Locate every blood parasite and identify its species.
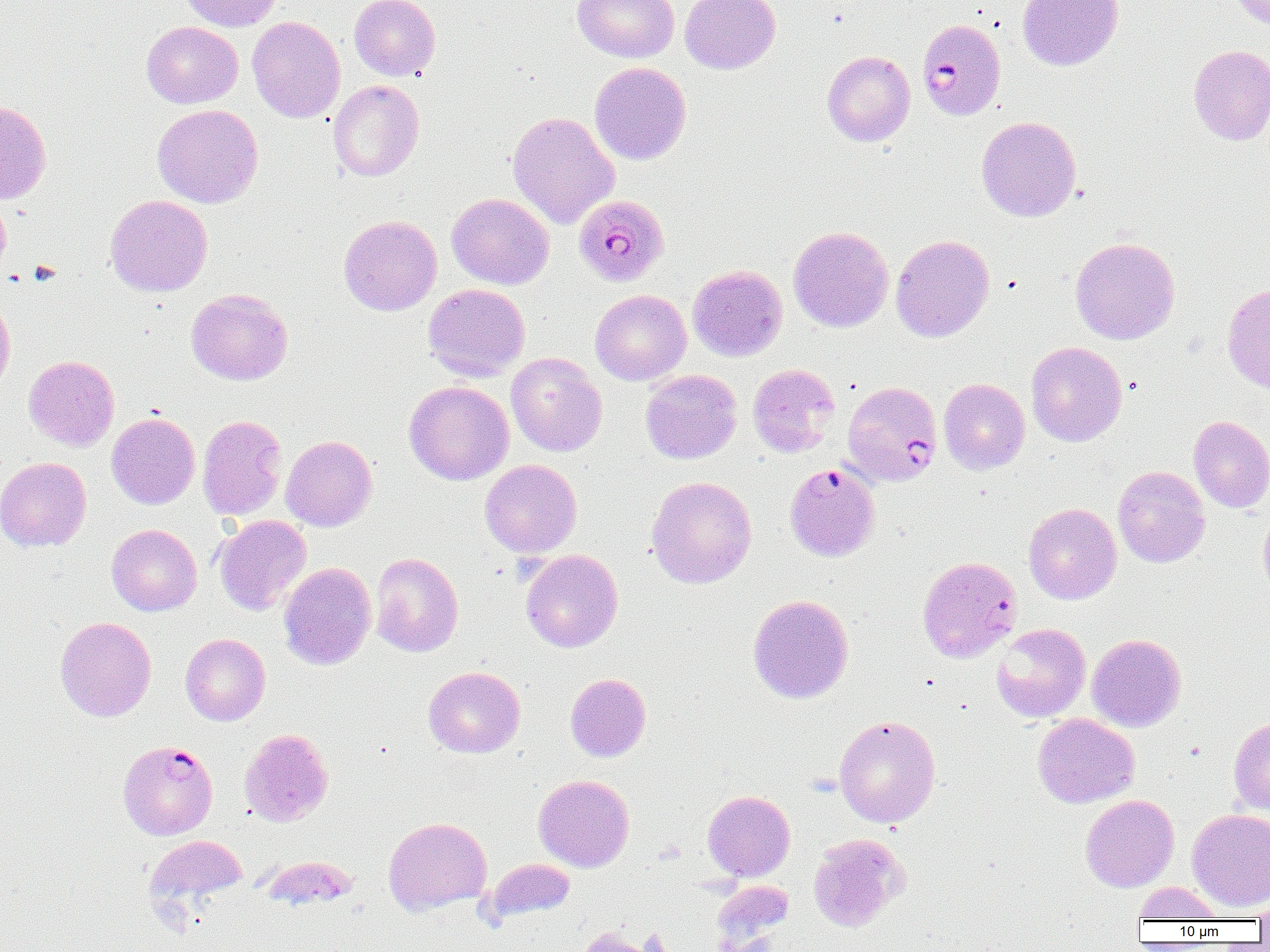
Approximate bounding boxes as [x1, y1, x2, y2] in pixels.
Plasmodium falciparum-infected red blood cells: [917, 19, 1006, 120], [574, 194, 669, 287], [842, 380, 943, 487], [784, 463, 880, 562], [917, 556, 1022, 662], [117, 740, 218, 840].
No Plasmodium ovale, Plasmodium malariae, Plasmodium vivax, Babesia divergens, or Trypanosoma brucei observed.

Summary:
  - Uninfected red blood cell locations: [180, 0, 281, 31], [349, 0, 440, 81], [572, 0, 679, 63], [680, 0, 781, 74], [1017, 0, 1123, 71], [1226, 0, 1270, 29], [247, 16, 345, 123], [141, 21, 243, 108], [1188, 45, 1270, 145], [822, 51, 915, 147], [590, 62, 691, 165], [328, 80, 424, 182], [0, 100, 52, 205], [152, 104, 263, 208], [508, 111, 619, 229], [976, 116, 1081, 222], [447, 192, 554, 289], [439, 193, 537, 381], [0, 194, 11, 280], [105, 194, 213, 297], [338, 215, 442, 316], [788, 226, 894, 332], [891, 234, 994, 342], [1070, 236, 1180, 345], [688, 265, 788, 362], [423, 283, 530, 382], [1222, 283, 1270, 395], [186, 288, 293, 385], [590, 289, 691, 386], [0, 294, 16, 402], [1026, 341, 1128, 447], [506, 352, 607, 456], [24, 355, 120, 451], [748, 364, 840, 457], [640, 369, 742, 464], [939, 378, 1030, 474], [404, 380, 514, 485], [106, 412, 200, 509], [198, 415, 287, 521], [1189, 415, 1270, 512], [281, 435, 377, 531], [0, 456, 91, 552], [480, 459, 582, 558], [1113, 466, 1210, 567], [646, 476, 757, 589], [1023, 503, 1122, 604], [1258, 506, 1270, 602], [214, 515, 312, 615], [106, 524, 202, 616], [521, 549, 623, 653], [370, 552, 463, 657], [278, 562, 376, 670], [747, 594, 854, 704], [55, 616, 156, 721], [991, 623, 1091, 722], [180, 633, 270, 726], [1087, 633, 1186, 731], [423, 666, 525, 758], [565, 673, 651, 761], [1032, 713, 1140, 808], [834, 714, 941, 828], [1229, 715, 1270, 816], [239, 728, 333, 826], [533, 774, 635, 872], [702, 790, 795, 881], [1080, 794, 1179, 892], [1187, 809, 1270, 911], [383, 817, 492, 914], [807, 834, 908, 932], [145, 835, 248, 912], [260, 855, 359, 911], [484, 858, 576, 925], [711, 879, 794, 950], [1132, 882, 1225, 921], [1251, 894, 1270, 925], [575, 925, 669, 952]
  - Slide-level diagnosis: Plasmodium falciparum
  - Magnification: 1000x
  - Image size: 1270×952 pixels
  - Field of view: single
  - Modality: optical microscopy
  - Preparation: thin blood smear